State which parasite is depicted.
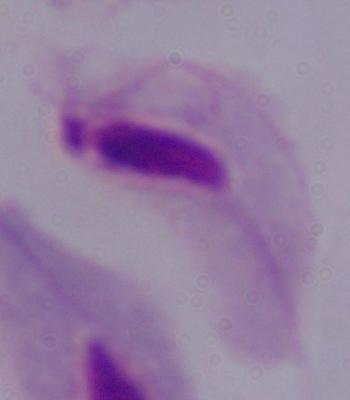
A trichomonad.

{
  "modality": "photomicrograph",
  "magnification": "1000x"
}